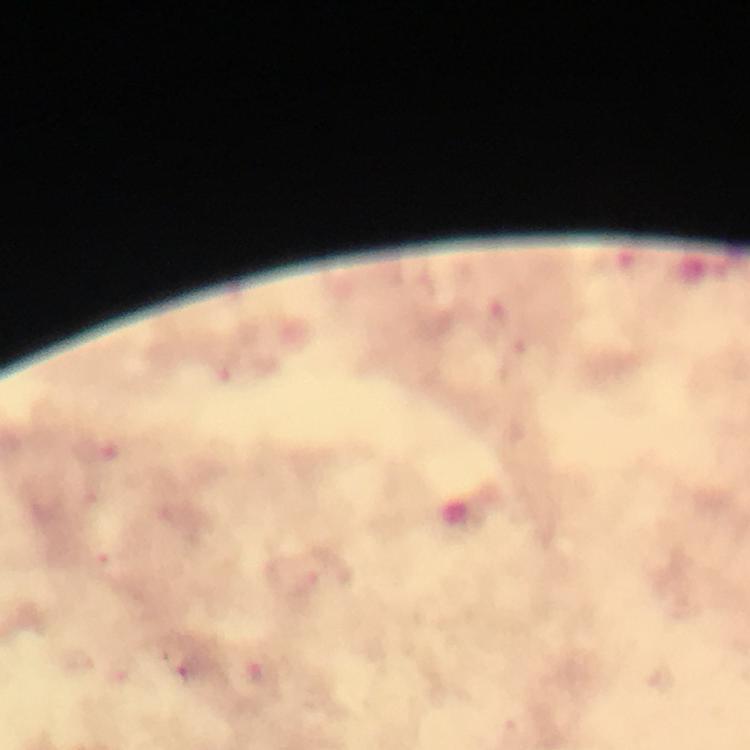
{
  "capture": "smartphone photograph through a microscope",
  "stain": "Giemsa",
  "immersion_oil": "used",
  "image_size": "750×750 pixels",
  "cropped_from": "a single field of view",
  "magnification": "100x",
  "malaria_parasite_locations": "approximate object centers, in pixels from the top-left corner: (x=260, y=672), (x=190, y=675)",
  "context": "from a diagnostic examination for malaria",
  "preparation": "thick blood film"
}